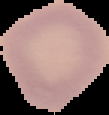

preparation: thin blood film
malaria_status: uninfected
image_type: segmented cell region on a black background
image_size: 109×115 pixels